Locate and identify every blood parasite.
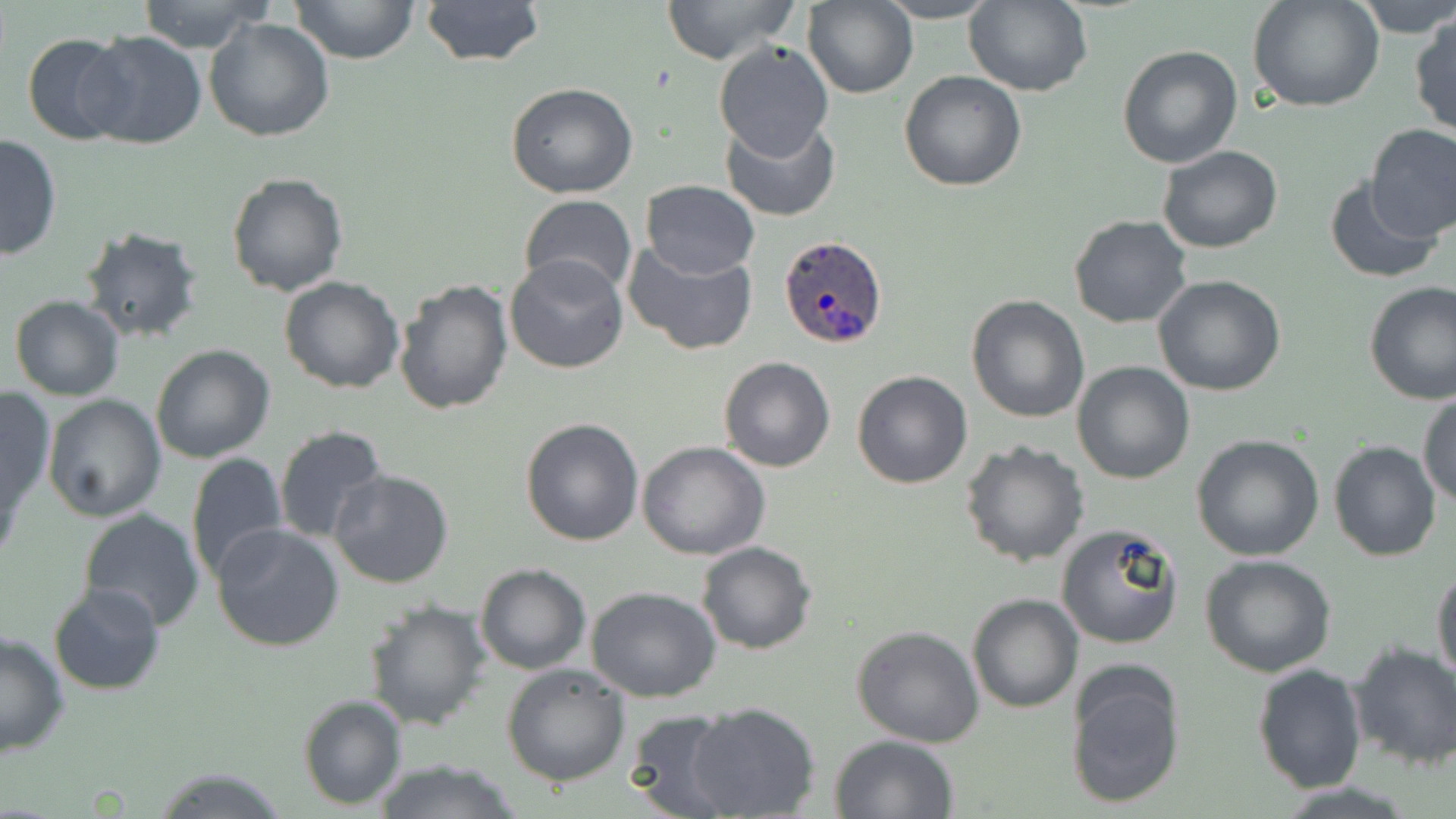

Approximate bounding boxes as (x1, y1, x2, y2) in pixels.
Plasmodium ovale-infected red blood cells: (777, 235, 888, 351).
No Plasmodium falciparum, Plasmodium malariae, Plasmodium vivax, Babesia divergens, or Trypanosoma brucei observed.

Summary:
  - Uninfected red blood cell locations: (135, 0, 275, 54), (290, 0, 420, 66), (417, 0, 546, 68), (660, 0, 802, 66), (873, 0, 1004, 23), (1351, 0, 1456, 39), (802, 1, 919, 99), (964, 1, 1093, 98), (1249, 1, 1386, 111), (1410, 11, 1455, 139), (203, 17, 335, 141), (78, 32, 209, 150), (22, 33, 135, 145), (712, 38, 835, 159), (1117, 44, 1242, 169), (899, 71, 1026, 191), (506, 83, 638, 199), (719, 115, 840, 221), (1365, 122, 1456, 241), (0, 133, 61, 261), (1158, 145, 1284, 254), (225, 171, 347, 297), (1323, 176, 1443, 284), (641, 180, 760, 279), (517, 196, 637, 298), (1068, 215, 1193, 328), (76, 226, 205, 346), (622, 239, 761, 356), (505, 255, 629, 374), (1152, 274, 1286, 396), (278, 275, 404, 393), (392, 277, 513, 416), (1363, 282, 1456, 405), (8, 295, 125, 401), (966, 296, 1090, 423), (150, 344, 276, 464), (718, 356, 837, 473), (1071, 361, 1196, 484), (851, 369, 973, 489), (0, 386, 55, 521), (1417, 392, 1456, 509), (42, 395, 165, 522), (519, 417, 645, 545), (273, 424, 390, 545), (1192, 434, 1325, 561), (959, 440, 1090, 569), (1328, 440, 1441, 561), (637, 441, 769, 560), (185, 452, 288, 583), (328, 469, 456, 589), (77, 510, 204, 632), (212, 523, 345, 649), (1055, 523, 1185, 650), (697, 540, 818, 655), (1199, 553, 1337, 677), (473, 563, 592, 676), (1432, 566, 1456, 686), (47, 583, 165, 697), (584, 585, 722, 703), (966, 592, 1082, 713), (361, 599, 490, 732), (852, 626, 985, 748), (0, 629, 70, 759), (1348, 641, 1456, 771), (1253, 661, 1366, 795), (502, 662, 632, 786), (1065, 662, 1187, 812), (297, 694, 407, 808), (686, 702, 822, 818), (622, 710, 742, 819), (829, 733, 958, 818), (368, 759, 528, 818), (151, 766, 292, 819)
  - Slide-level diagnosis: Plasmodium ovale
  - Field of view: one of a larger specimen
  - Image size: 1456×819 pixels
  - Preparation: thin blood smear
  - Modality: optical microscopy
  - Magnification: 1000x
  - Stain: May-Grünwald-Giemsa